State which parasite is depicted.
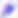
Toxoplasma gondii.

400x magnification. Micrograph.